Report the malaria status of this cell.
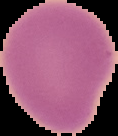
It is uninfected.

preparation = thin blood smear
image type = segmented cell region on a black background
image size = 118×136 pixels